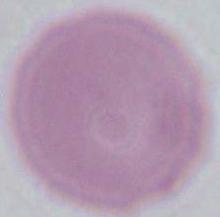

Summary:
  - Modality: photomicrograph
  - Magnification: 1000x
  - Identification: erythrocyte